Outline each blood parasite and name the species.
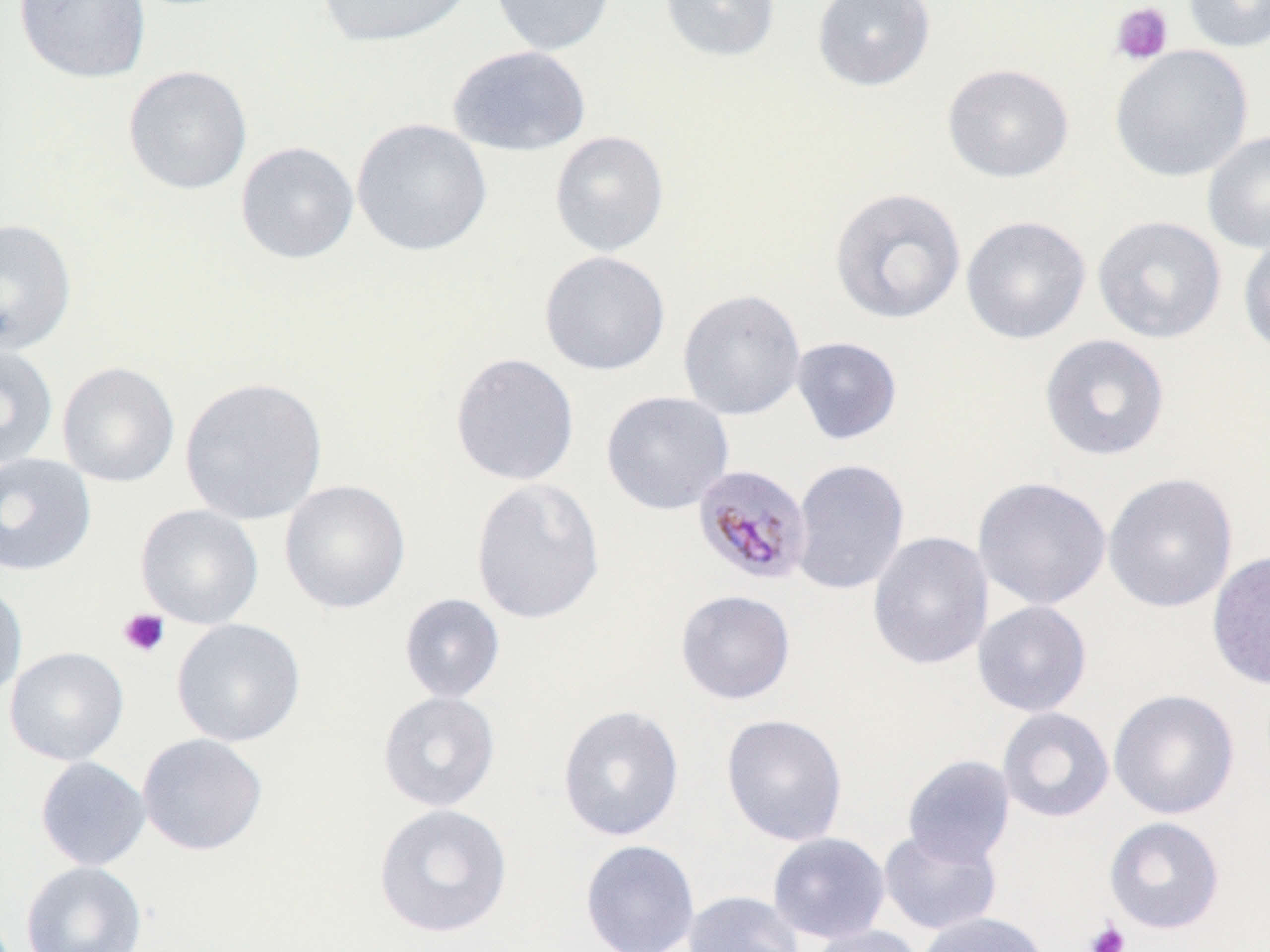
Approximate bounding boxes as (x1, y1, x2, y2) in pixels.
Plasmodium malariae-infected red blood cells: (692, 464, 812, 586).
No Plasmodium falciparum, Plasmodium ovale, Plasmodium vivax, Babesia divergens, or Trypanosoma brucei observed.

Summary:
  - Platelet locations: (1110, 2, 1174, 66), (118, 609, 170, 658), (1084, 919, 1130, 952)
  - Uninfected red blood cell locations: (14, 0, 151, 83), (315, 0, 474, 47), (490, 0, 617, 56), (658, 0, 781, 62), (812, 0, 935, 91), (1183, 0, 1270, 53), (447, 45, 591, 157), (1109, 45, 1253, 182), (942, 63, 1074, 182), (123, 65, 252, 195), (351, 118, 493, 256), (1202, 129, 1270, 254), (549, 130, 670, 257), (235, 141, 359, 264), (829, 187, 967, 325), (1092, 214, 1227, 344), (960, 215, 1092, 345), (0, 218, 77, 356), (1237, 232, 1270, 357), (539, 250, 671, 376), (677, 289, 806, 421), (1039, 333, 1171, 462), (790, 336, 903, 445), (0, 344, 58, 470), (449, 352, 580, 486), (57, 361, 180, 487), (178, 376, 328, 525), (601, 390, 734, 515), (0, 452, 97, 576), (790, 458, 909, 595), (1103, 472, 1239, 613), (973, 476, 1112, 610), (470, 477, 606, 625), (279, 479, 411, 614), (135, 503, 264, 628), (868, 531, 993, 670), (1206, 550, 1270, 692), (0, 581, 28, 702), (675, 590, 796, 705), (398, 592, 506, 703), (972, 600, 1092, 717), (171, 617, 306, 747), (5, 646, 129, 766), (1108, 689, 1240, 820), (377, 690, 501, 812), (557, 704, 685, 842), (997, 707, 1114, 823), (720, 713, 848, 846), (136, 732, 268, 856), (902, 755, 1016, 866), (35, 756, 151, 871), (373, 803, 513, 938), (1104, 816, 1225, 934), (878, 828, 1002, 935), (767, 832, 891, 943), (579, 839, 700, 952), (20, 860, 147, 952), (683, 890, 804, 952), (914, 911, 1050, 952), (805, 924, 925, 952)
  - Slide-level diagnosis: Plasmodium malariae
  - Image size: 1270×952 pixels
  - Field of view: one of a larger specimen
  - Stain: May-Grünwald-Giemsa
  - Modality: light microscopy
  - Magnification: 1000x
  - Preparation: thin blood film